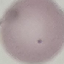
Malaria status: uninfected. Photographed with a smartphone camera at the microscope eyepiece. Cell patch, automatically extracted from a larger field of view and resized to 64 × 64 pixels. Thin blood film. Giemsa stain.